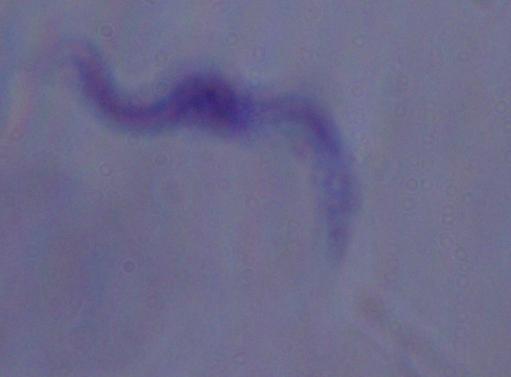

modality: photomicrograph
identification: trypanosome
magnification: 1000x